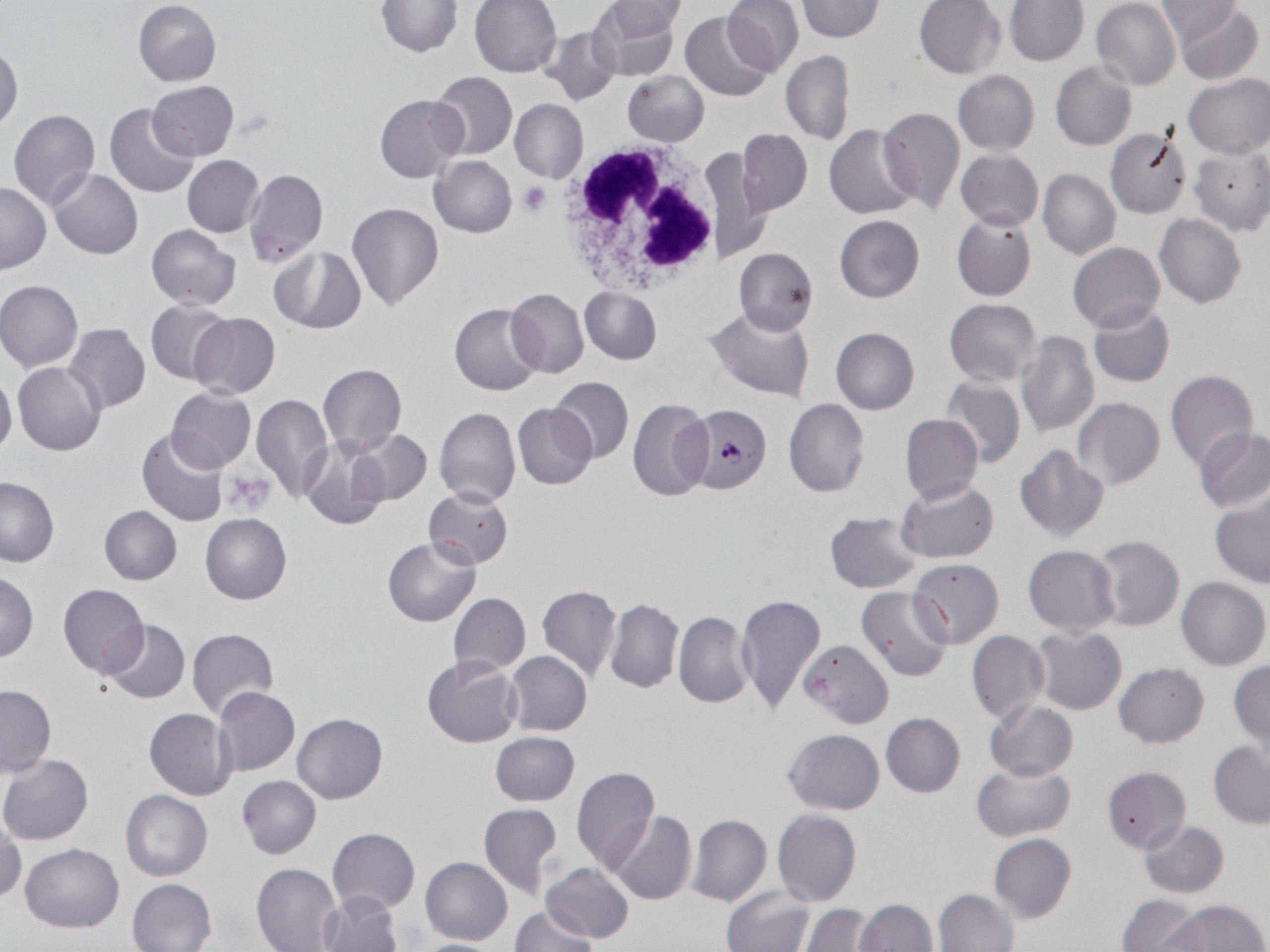
{
  "slide_level_diagnosis": "Plasmodium falciparum",
  "image_size": "1270×952 pixels",
  "magnification": "1000x",
  "modality": "optical microscopy",
  "stain": "May-Grünwald-Giemsa",
  "plasmodium_falciparum_infected_red_blood_cell_locations": "approximate bounding boxes as [x1, y1, x2, y2] in pixels: [666, 411, 767, 503]",
  "preparation": "thin blood smear",
  "uninfected_red_blood_cell_locations": "approximate bounding boxes as [x1, y1, x2, y2] in pixels: [470, 0, 560, 76], [589, 0, 681, 81], [723, 0, 804, 75], [797, 0, 885, 43], [914, 0, 1005, 78], [1004, 0, 1089, 65], [1092, 0, 1180, 90], [1156, 0, 1238, 43], [133, 1, 221, 86], [377, 1, 462, 56], [604, 1, 688, 37], [1174, 3, 1264, 84], [680, 12, 775, 101], [538, 25, 620, 104], [0, 45, 23, 133], [782, 51, 854, 145], [1050, 62, 1136, 150], [429, 70, 516, 160], [624, 71, 709, 146], [953, 71, 1039, 154], [1183, 73, 1269, 158], [148, 81, 239, 161], [375, 94, 466, 182], [509, 98, 588, 183], [105, 102, 200, 198], [877, 106, 965, 218], [8, 109, 101, 210], [825, 124, 918, 218], [1104, 126, 1192, 218], [737, 129, 812, 216], [699, 143, 771, 267], [1190, 146, 1270, 235], [956, 148, 1043, 229], [182, 155, 264, 237], [429, 155, 517, 237], [48, 168, 142, 259], [243, 168, 328, 267], [1038, 168, 1120, 259], [1, 182, 50, 273], [347, 202, 443, 311], [951, 212, 1036, 302], [1155, 213, 1247, 307], [834, 215, 924, 302], [147, 223, 241, 310], [1069, 242, 1163, 332], [734, 246, 817, 334], [268, 247, 365, 334], [0, 279, 83, 372], [580, 286, 662, 364], [505, 287, 589, 379], [944, 299, 1040, 385], [145, 300, 235, 385], [449, 303, 544, 395], [1088, 303, 1174, 388], [703, 307, 814, 401], [189, 312, 280, 399], [64, 322, 150, 414], [831, 327, 919, 413], [1016, 332, 1098, 438], [13, 362, 106, 456], [316, 363, 407, 453], [0, 368, 16, 459], [1165, 369, 1258, 471], [941, 375, 1025, 469], [551, 377, 632, 461], [166, 387, 255, 473], [251, 394, 333, 501], [627, 397, 713, 501], [1073, 397, 1164, 489], [784, 398, 868, 496], [512, 402, 597, 489], [435, 407, 521, 507], [900, 414, 982, 503], [346, 427, 432, 508], [1195, 427, 1270, 512], [136, 428, 230, 528], [299, 434, 394, 530], [1015, 445, 1108, 542], [0, 477, 59, 566], [897, 478, 998, 562], [423, 487, 513, 569], [1210, 495, 1270, 588], [99, 505, 182, 584], [825, 512, 922, 594], [201, 513, 291, 604], [1091, 535, 1184, 630], [383, 537, 480, 626], [1023, 546, 1119, 635], [909, 559, 1003, 648], [0, 571, 38, 662], [1177, 576, 1269, 669], [58, 584, 148, 678], [537, 585, 621, 682], [856, 586, 953, 680], [448, 593, 531, 675], [736, 594, 826, 715], [604, 598, 683, 693], [673, 611, 754, 708], [103, 620, 189, 703], [1032, 626, 1126, 715], [186, 627, 279, 720], [967, 631, 1050, 723], [800, 640, 892, 728], [505, 651, 592, 736], [421, 656, 522, 748], [1229, 660, 1269, 751], [1114, 663, 1208, 747], [0, 685, 55, 775], [214, 687, 299, 776], [984, 700, 1078, 781], [144, 709, 236, 800], [292, 712, 386, 803], [881, 713, 965, 796], [785, 728, 883, 814], [490, 732, 580, 805], [1208, 740, 1270, 828], [0, 754, 93, 844], [974, 763, 1074, 841], [1101, 766, 1191, 853], [571, 767, 659, 872], [237, 775, 321, 858], [120, 790, 212, 881], [479, 802, 561, 898], [608, 809, 696, 904], [773, 810, 861, 907], [687, 813, 771, 906], [0, 815, 25, 902], [1140, 821, 1230, 897], [328, 827, 420, 914], [988, 834, 1077, 922], [20, 843, 124, 931], [420, 856, 512, 945], [543, 862, 634, 942], [252, 863, 340, 952], [127, 878, 216, 952], [722, 885, 814, 952], [933, 889, 1017, 952], [318, 890, 403, 952], [1118, 894, 1203, 952], [853, 899, 937, 951], [1164, 899, 1267, 951], [800, 904, 877, 952], [509, 906, 596, 952], [408, 939, 511, 951]",
  "platelet_locations": "approximate bounding boxes as [x1, y1, x2, y2] in pixels: [520, 183, 551, 216], [225, 470, 277, 514]",
  "field_of_view": "one of a larger specimen",
  "white_blood_cell_locations": "approximate bounding boxes as [x1, y1, x2, y2] in pixels: [557, 137, 730, 295]"
}